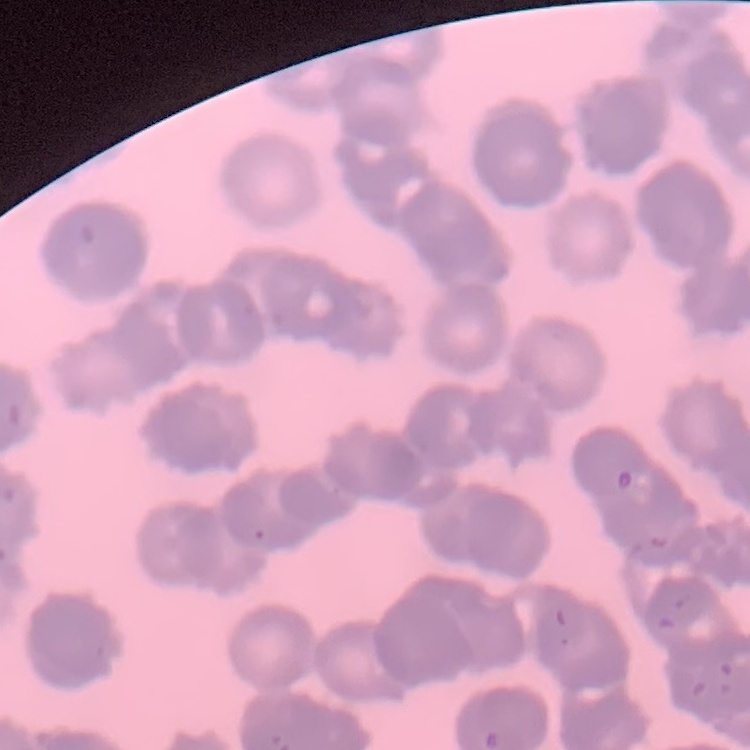 The erythrocytes show rouleaux formation. Thin blood smear. Stained with either Field's or Giemsa. Square crop of a larger photomicrograph.